Locate and identify every blood parasite.
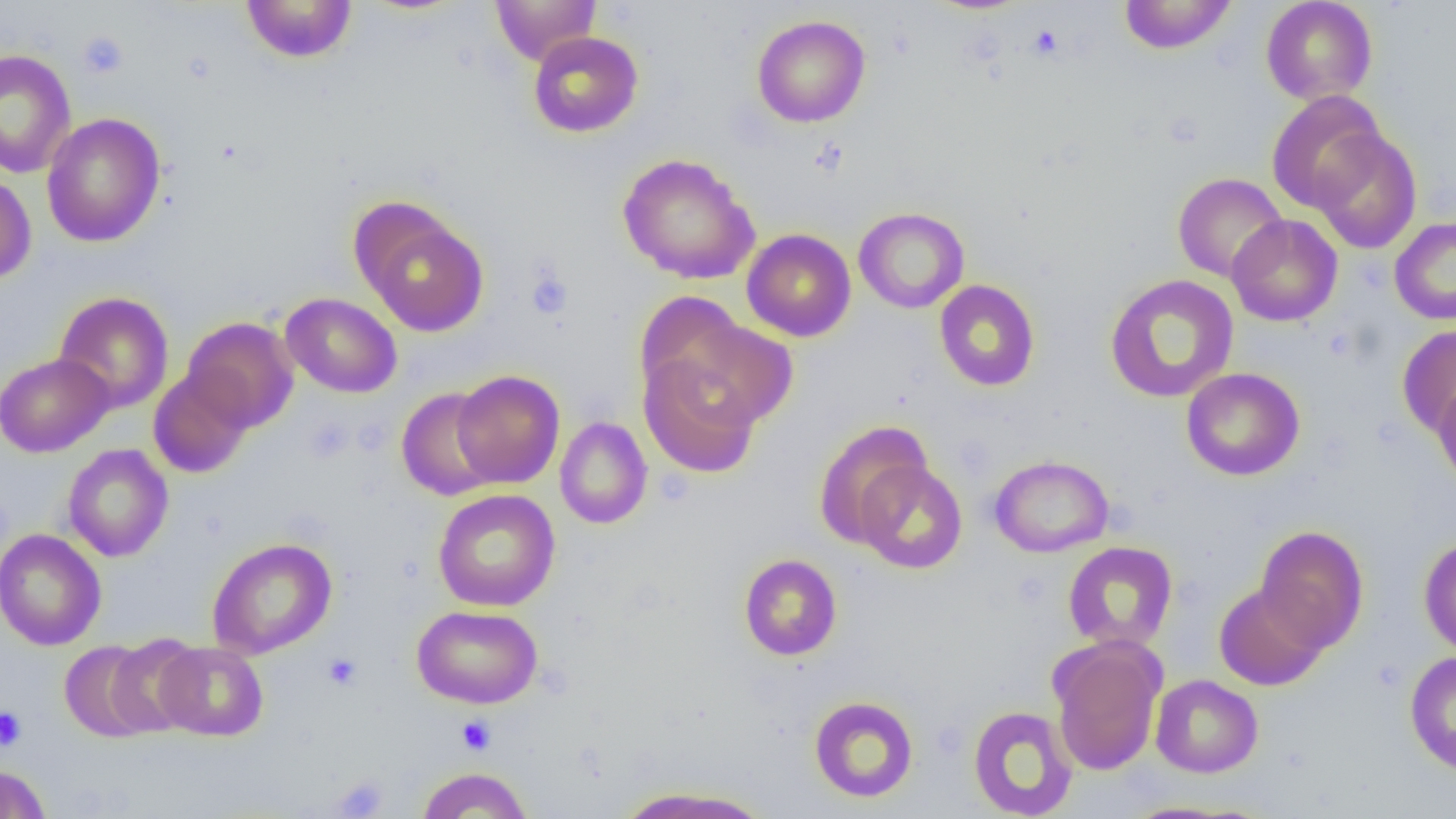

No blood parasites seen.

Approximate bounding boxes as [x1, y1, x2, y2] in pixels. Platelet locations: [1027, 25, 1063, 60], [77, 30, 129, 79], [525, 268, 573, 319], [322, 653, 362, 690], [0, 706, 27, 752], [456, 715, 495, 755]. Uninfected red blood cell locations: [490, 0, 601, 66], [1119, 0, 1237, 55], [1260, 0, 1378, 106], [241, 1, 358, 64], [751, 15, 871, 128], [528, 31, 643, 138], [0, 49, 76, 178], [1266, 90, 1387, 213], [42, 113, 166, 247], [1309, 128, 1422, 255], [617, 153, 761, 284], [0, 171, 36, 284], [1172, 172, 1288, 283], [354, 203, 489, 337], [854, 207, 969, 313], [1227, 214, 1343, 327], [1389, 217, 1456, 324], [742, 228, 856, 342], [1104, 274, 1240, 403], [934, 280, 1040, 392], [53, 291, 174, 414], [280, 292, 403, 398], [635, 293, 757, 414], [664, 315, 799, 429], [182, 316, 298, 432], [1397, 324, 1456, 438], [0, 352, 113, 457], [639, 354, 762, 478], [1180, 367, 1305, 481], [148, 368, 254, 479], [451, 369, 565, 488], [1433, 376, 1456, 491], [397, 387, 503, 501], [555, 416, 652, 529], [813, 421, 933, 549], [62, 444, 174, 562], [988, 454, 1114, 557], [854, 460, 968, 573], [432, 489, 561, 612], [1255, 524, 1368, 654], [0, 529, 106, 651], [1419, 536, 1456, 657], [207, 537, 337, 660], [1062, 541, 1178, 651], [738, 553, 842, 660], [1214, 582, 1327, 690], [412, 605, 543, 709], [104, 633, 204, 737], [1048, 637, 1166, 776], [59, 640, 161, 742], [155, 641, 268, 741], [1403, 650, 1456, 776], [1150, 674, 1263, 778], [809, 695, 919, 802], [967, 705, 1078, 818], [0, 764, 51, 819], [415, 766, 532, 818], [614, 785, 773, 819]. Slide-level diagnosis: negative for blood parasites. One field of a larger specimen. Optical microscopy. Thin blood smear. 1000x magnification. Image is 1456×819 pixels.